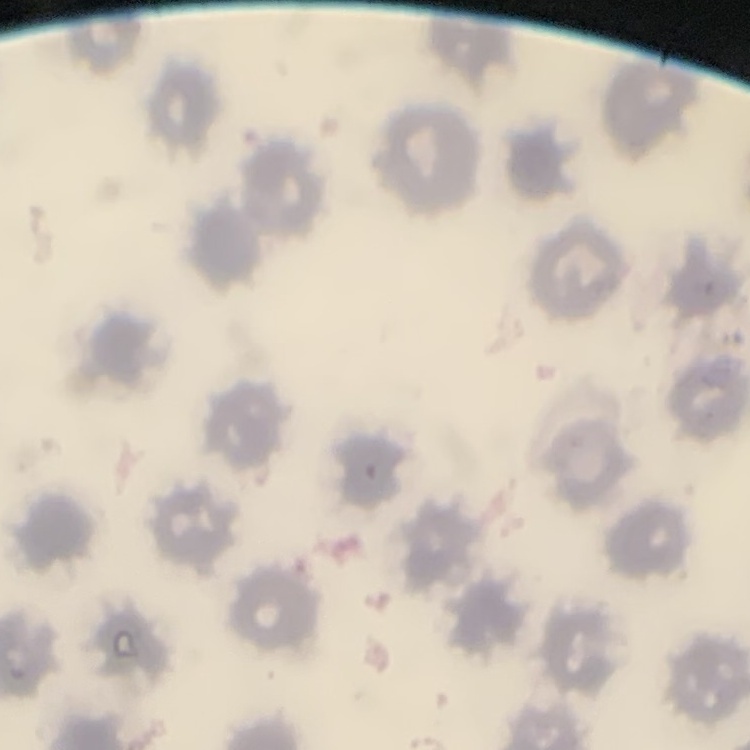
erythrocyte morphology = no rouleaux formation
stain = Field's or Giemsa
image type = one tile cut from a larger photomicrograph
preparation = thin peripheral smear